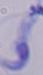

Summary:
  - Identification: trypanosome
  - Magnification: 1000x
  - Modality: photomicrograph